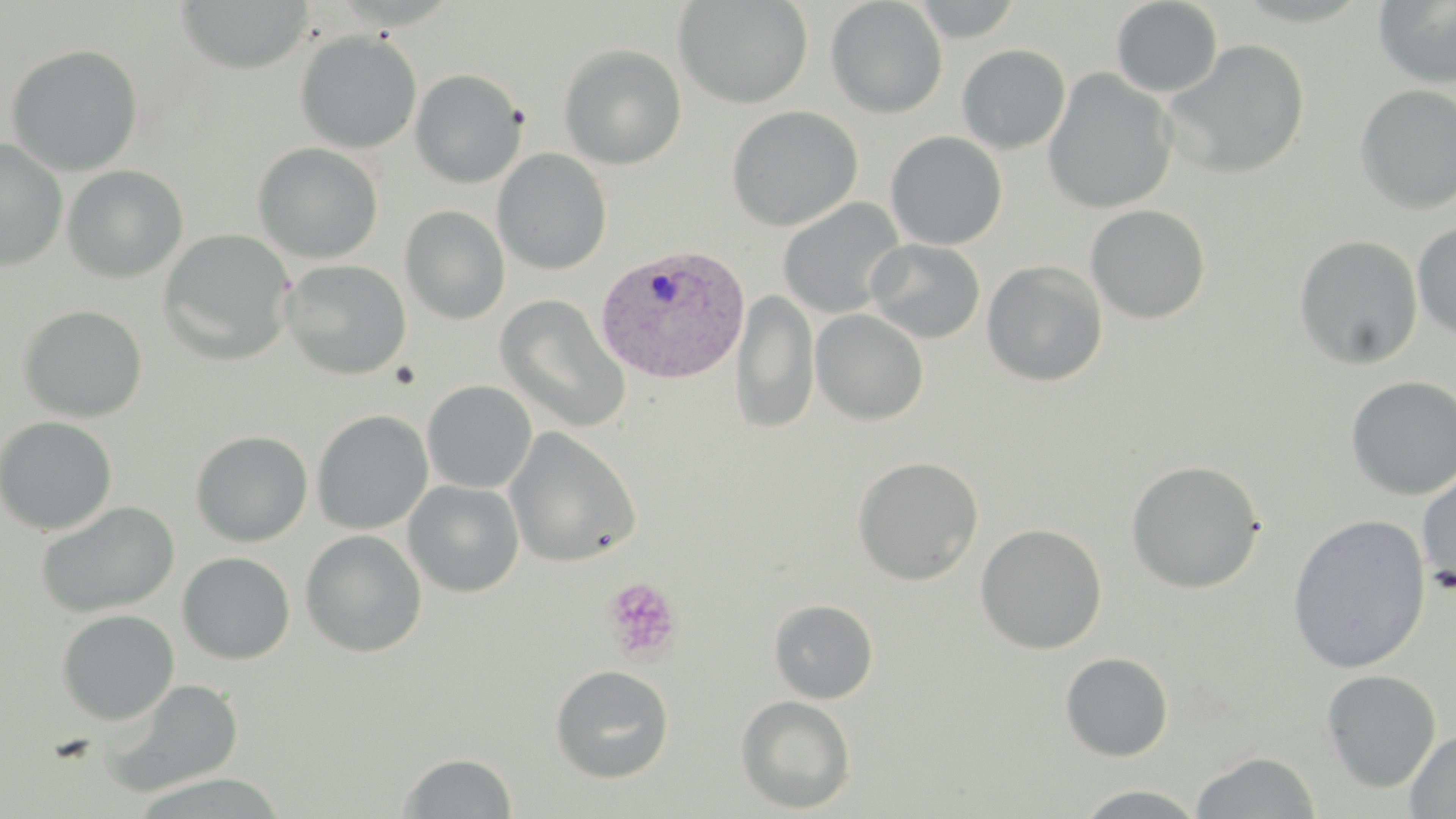

Approximate bounding boxes as named x1/y1/x2/y2 corners in pixels. Platelet locations: (x1=391, y1=362, x2=421, y2=390), (x1=603, y1=577, x2=682, y2=663). Plasmodium vivax-infected red blood cell locations: (x1=594, y1=244, x2=750, y2=385). Uninfected red blood cell locations: (x1=673, y1=0, x2=812, y2=109), (x1=825, y1=0, x2=947, y2=118), (x1=909, y1=0, x2=1023, y2=41), (x1=1373, y1=0, x2=1456, y2=88), (x1=174, y1=1, x2=313, y2=74), (x1=1111, y1=1, x2=1223, y2=97), (x1=295, y1=31, x2=421, y2=153), (x1=1163, y1=39, x2=1310, y2=179), (x1=5, y1=44, x2=143, y2=176), (x1=559, y1=44, x2=687, y2=169), (x1=957, y1=44, x2=1071, y2=153), (x1=1042, y1=68, x2=1178, y2=215), (x1=410, y1=69, x2=526, y2=188), (x1=1354, y1=84, x2=1456, y2=215), (x1=727, y1=106, x2=862, y2=231), (x1=884, y1=133, x2=1005, y2=251), (x1=0, y1=138, x2=68, y2=271), (x1=253, y1=142, x2=383, y2=263), (x1=493, y1=148, x2=612, y2=275), (x1=62, y1=165, x2=188, y2=283), (x1=778, y1=198, x2=906, y2=318), (x1=800, y1=198, x2=916, y2=426), (x1=1085, y1=204, x2=1211, y2=323), (x1=400, y1=206, x2=510, y2=324), (x1=1412, y1=221, x2=1456, y2=340), (x1=159, y1=229, x2=296, y2=364), (x1=1294, y1=235, x2=1423, y2=370), (x1=865, y1=239, x2=985, y2=343), (x1=280, y1=259, x2=412, y2=379), (x1=982, y1=260, x2=1108, y2=386), (x1=731, y1=289, x2=820, y2=435), (x1=495, y1=294, x2=631, y2=434), (x1=18, y1=305, x2=148, y2=423), (x1=810, y1=309, x2=929, y2=425), (x1=1345, y1=375, x2=1456, y2=501), (x1=422, y1=380, x2=537, y2=493), (x1=311, y1=410, x2=433, y2=535), (x1=0, y1=416, x2=117, y2=536), (x1=504, y1=427, x2=641, y2=567), (x1=190, y1=430, x2=313, y2=546), (x1=852, y1=456, x2=984, y2=585), (x1=1126, y1=459, x2=1265, y2=593), (x1=1416, y1=469, x2=1456, y2=597), (x1=404, y1=479, x2=525, y2=597), (x1=35, y1=501, x2=179, y2=618), (x1=1287, y1=513, x2=1431, y2=674), (x1=974, y1=523, x2=1107, y2=654), (x1=300, y1=529, x2=427, y2=656), (x1=177, y1=551, x2=295, y2=664), (x1=769, y1=599, x2=878, y2=704), (x1=56, y1=609, x2=179, y2=725), (x1=1060, y1=653, x2=1174, y2=761), (x1=550, y1=664, x2=675, y2=782), (x1=1320, y1=669, x2=1441, y2=793), (x1=102, y1=679, x2=244, y2=798), (x1=736, y1=695, x2=856, y2=814), (x1=1405, y1=729, x2=1456, y2=818), (x1=1190, y1=751, x2=1321, y2=818), (x1=398, y1=752, x2=517, y2=817), (x1=1072, y1=785, x2=1208, y2=818). Slide-level diagnosis: Plasmodium vivax. Captured at 1000x magnification. One field of a larger specimen. Thin blood film. May-Grünwald-Giemsa stain. Image is 1456×819 pixels. Light microscopy.